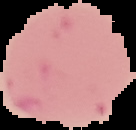
Summary:
  - Preparation: thin blood film
  - Image type: cell region segmented out of the field of view; surrounding area masked to black
  - Image size: 136×130 pixels
  - Malaria status: uninfected